Identify the blood parasite species.
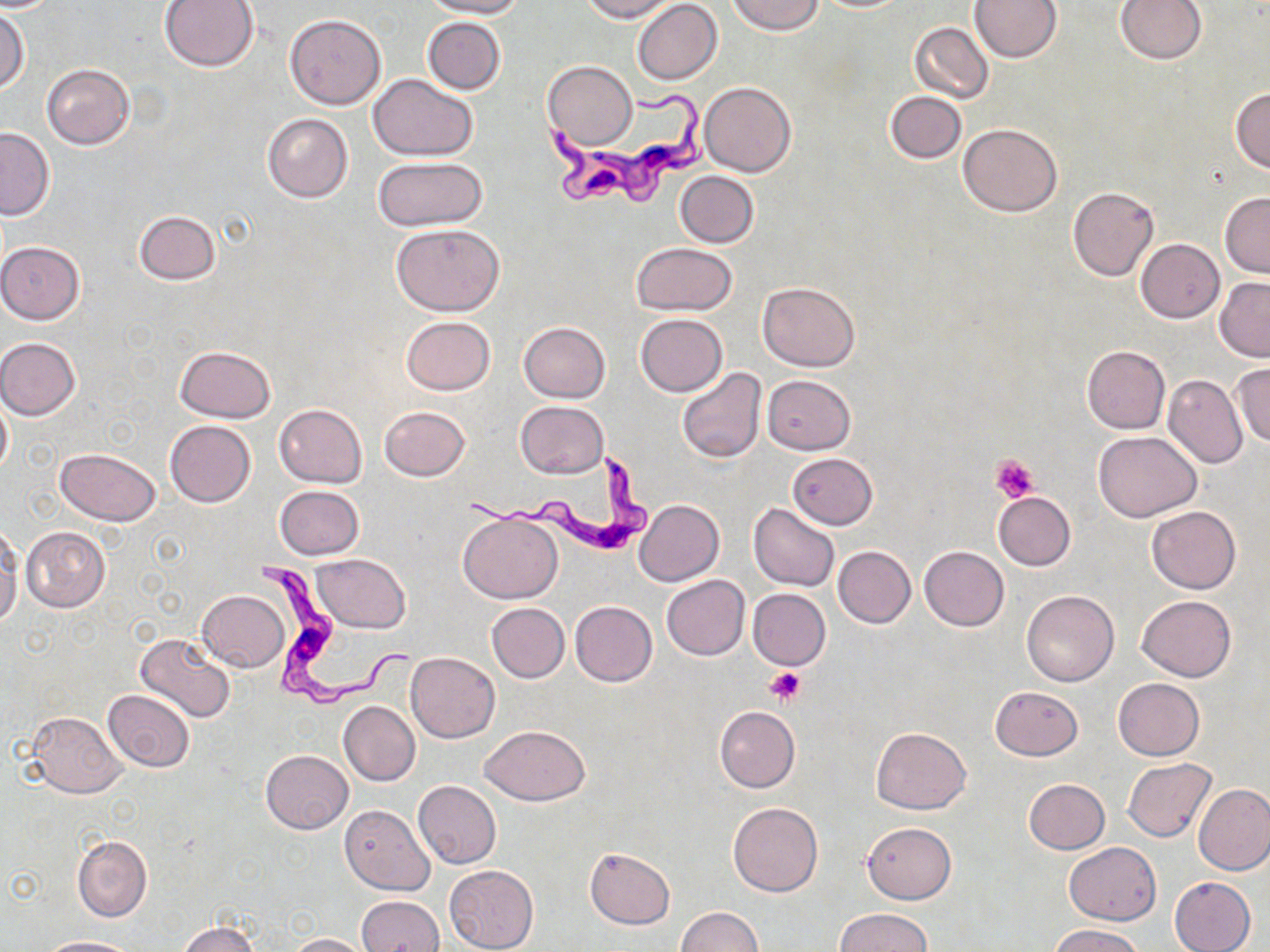
Trypanosoma brucei.

Approximate bounding boxes as (x1,y1)-(x2,y2) corner pairs in pixels. Uninfected red blood cell locations: (159,0)-(261,73), (420,0)-(524,18), (578,0)-(679,22), (728,0)-(824,35), (970,0)-(1062,62), (1115,0)-(1208,64), (631,1)-(722,85), (1,9)-(29,94), (284,14)-(386,110), (422,17)-(505,95), (909,21)-(993,103), (543,60)-(637,151), (42,64)-(134,149), (368,74)-(476,160), (700,82)-(796,176), (1229,87)-(1269,173), (885,91)-(965,164), (261,113)-(352,203), (958,123)-(1062,216), (1,127)-(54,219), (374,156)-(488,232), (676,171)-(758,248), (1068,187)-(1159,281), (1220,193)-(1270,277), (135,211)-(221,285), (391,223)-(504,316), (1135,239)-(1225,323), (0,242)-(85,324), (631,242)-(737,316), (1214,278)-(1270,361), (757,282)-(861,371), (635,313)-(728,397), (401,316)-(496,395), (518,322)-(610,402), (0,337)-(80,420), (175,344)-(275,422), (1082,346)-(1169,433), (1230,363)-(1270,447), (677,369)-(767,465), (1162,374)-(1247,468), (763,375)-(855,453), (0,392)-(12,478), (516,402)-(608,479), (273,404)-(367,488), (379,405)-(470,481), (164,420)-(256,507), (1093,430)-(1201,522), (54,448)-(161,526), (788,453)-(877,530), (275,484)-(363,560), (994,492)-(1075,570), (634,500)-(724,586), (750,502)-(839,591), (1147,506)-(1241,594), (458,512)-(561,604), (0,523)-(22,624), (20,526)-(109,611), (832,545)-(915,628), (919,545)-(1009,630), (311,553)-(410,633), (661,575)-(749,660), (748,589)-(830,670), (197,590)-(288,672), (1022,590)-(1119,687), (1137,594)-(1235,682), (569,600)-(657,686), (487,603)-(569,682), (135,632)-(237,723), (406,652)-(499,742), (1112,678)-(1205,761), (989,686)-(1083,761), (102,691)-(193,772), (338,702)-(420,786), (715,706)-(800,793), (25,711)-(125,798), (478,724)-(591,805), (870,727)-(971,815), (261,749)-(353,833), (1123,758)-(1217,842), (1024,779)-(1110,854), (413,781)-(502,867), (1194,783)-(1270,875), (339,803)-(435,895), (727,803)-(823,897), (862,821)-(955,903), (73,836)-(152,922), (1065,843)-(1161,925), (584,847)-(674,929), (444,865)-(539,952), (1169,875)-(1256,952), (356,895)-(445,952), (675,906)-(763,952), (836,908)-(933,952), (179,922)-(261,952), (1049,924)-(1142,952), (285,933)-(371,951), (37,936)-(139,952). Trypanosoma brucei locations: (539,87)-(716,208), (450,448)-(656,555), (252,555)-(414,713). Platelet locations: (990,454)-(1038,503), (766,667)-(806,705). Optical microscopy. May-Grünwald-Giemsa stain. 1000x magnification. Single field of view. Image is 1270×952 pixels. Thin blood film.